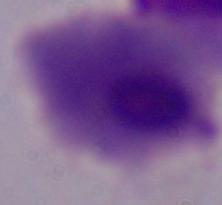

Micrograph. 1000x magnification. A trichomonad is shown.